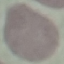

{
  "malaria_status": "uninfected",
  "image_type": "automatically extracted cell patch, resized to 64 × 64 pixels",
  "stain": "Giemsa",
  "preparation": "thin smear",
  "capture": "smartphone camera at the microscope eyepiece"
}